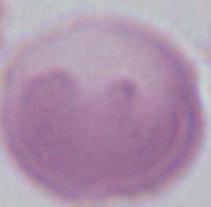

modality = photomicrograph
magnification = 1000x
identification = erythrocyte